Outline each Plasmodium falciparum parasite and classify it by life-cycle stage.
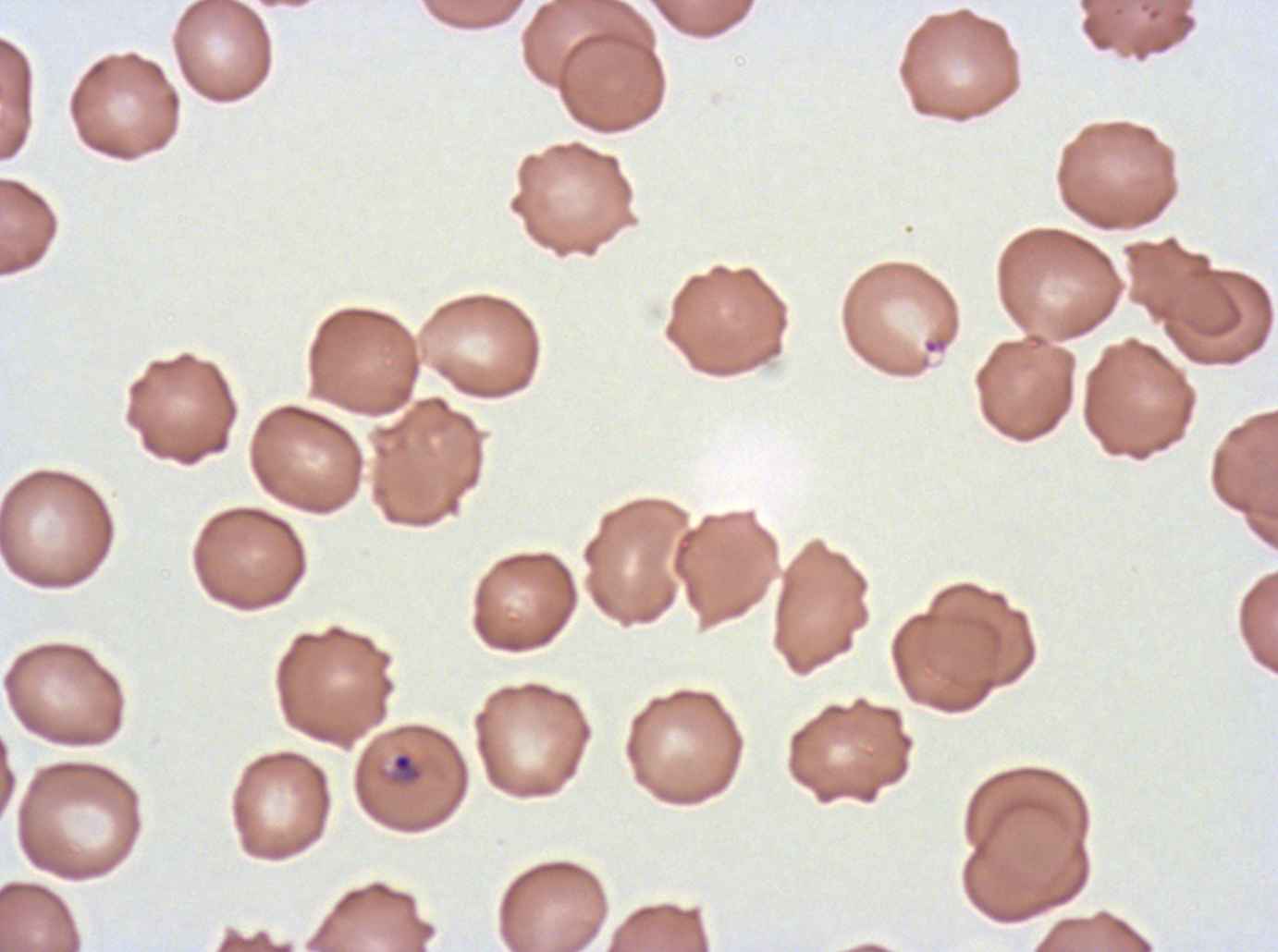

Approximate bounding boxes as (x1, y1, x2, y2) in pixels.
Rings: (391, 751, 423, 784).
No late-ring/early-trophozoite forms, mid trophozoites, late trophozoites, early schizonts, late schizonts, segmenters, or gametocytes observed.

Thin blood smear. Giemsa stain. Plasmodium falciparum from a patient in The Gambia, cultured ex vivo for 24 to 48 hours. Image is 1278×952 pixels. A sub-image separated from a larger composite.